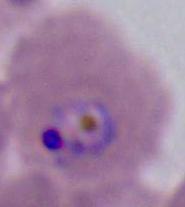

{
  "modality": "photomicrograph",
  "identification": "Plasmodium",
  "magnification": "400x or 1000x"
}